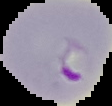

Summary:
  - Image size: 112×106 pixels
  - Malaria status: parasitized
  - Image type: segmented cell region on a black background
  - Preparation: thin blood film